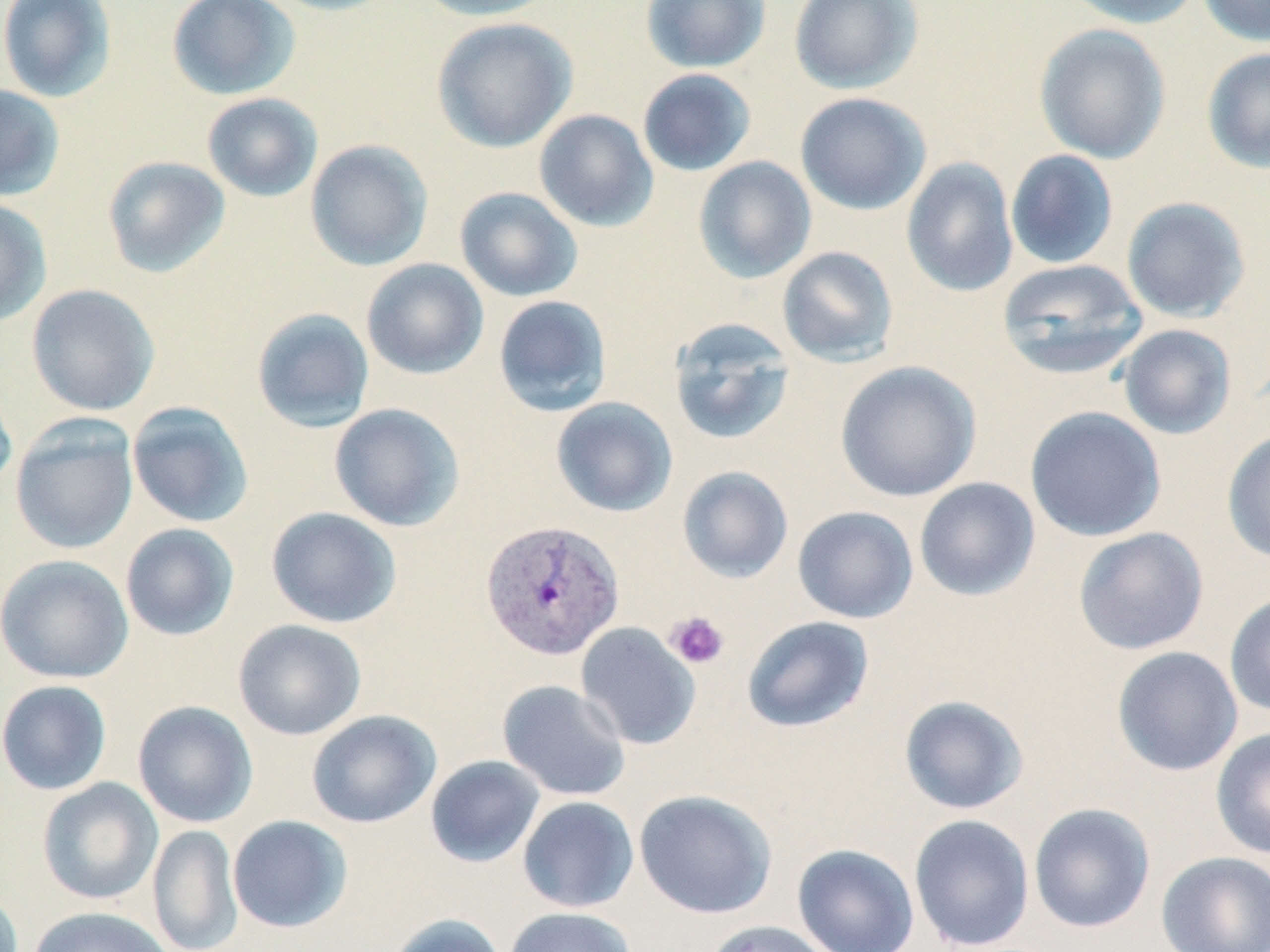
{
  "slide_level_diagnosis": "Plasmodium vivax",
  "stain": "May-Grünwald-Giemsa",
  "modality": "optical microscopy",
  "platelet_locations": "approximate bounding boxes as (x1,y1)-(x2,y2) corner pairs in pixels: (665,611)-(730,670)",
  "field_of_view": "one of a larger specimen",
  "plasmodium_vivax_infected_red_blood_cell_locations": "approximate bounding boxes as (x1,y1)-(x2,y2) corner pairs in pixels: (480,519)-(625,662)",
  "magnification": "1000x",
  "image_size": "1270×952 pixels",
  "preparation": "thin blood film",
  "uninfected_red_blood_cell_locations": "approximate bounding boxes as (x1,y1)-(x2,y2) corner pairs in pixels: (0,0)-(118,103), (166,0)-(301,101), (261,0)-(398,16), (414,0)-(558,21), (640,0)-(771,73), (789,0)-(922,94), (1063,0)-(1204,29), (1197,0)-(1270,46), (431,17)-(577,153), (1034,23)-(1171,164), (1201,46)-(1270,174), (637,68)-(757,177), (0,84)-(65,202), (794,92)-(931,215), (202,93)-(323,203), (533,109)-(659,232), (304,139)-(434,272), (1005,149)-(1119,270), (102,156)-(230,278), (693,156)-(817,284), (901,157)-(1019,297), (454,186)-(583,302), (0,197)-(52,327), (1121,197)-(1251,323), (777,245)-(899,367), (360,258)-(489,380), (997,258)-(1148,380), (26,283)-(160,416), (493,294)-(612,417), (251,307)-(375,433), (668,318)-(797,446), (1117,324)-(1237,440), (835,361)-(982,502), (0,372)-(17,496), (551,397)-(678,517), (127,401)-(254,528), (329,403)-(465,532), (1025,406)-(1167,542), (10,417)-(139,555), (1222,426)-(1270,565), (677,466)-(794,584), (914,477)-(1040,601), (792,506)-(919,624), (266,507)-(402,629), (120,523)-(239,641), (1073,526)-(1209,655), (1,554)-(133,683), (1224,591)-(1270,718), (742,615)-(875,733), (233,619)-(367,740), (575,622)-(701,750), (1111,646)-(1244,777), (497,679)-(631,801), (0,680)-(112,795), (899,695)-(1029,814), (133,700)-(258,828), (306,710)-(442,828), (1210,726)-(1270,860), (425,755)-(545,868), (37,777)-(163,905), (634,789)-(777,918), (517,796)-(639,913), (1028,802)-(1156,934), (909,814)-(1035,952), (227,815)-(353,933), (147,824)-(243,952), (792,843)-(920,952), (1155,851)-(1270,952), (0,886)-(24,952), (27,906)-(175,952), (503,906)-(636,952), (384,913)-(508,952), (703,920)-(838,952)"
}